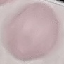

result = negative for malaria parasites
image type = cell patch, automatically extracted from a larger field of view and resized to 64 × 64 pixels
capture = smartphone camera at the microscope eyepiece
preparation = thin smear
stain = Giemsa